Locate and identify every blood parasite.
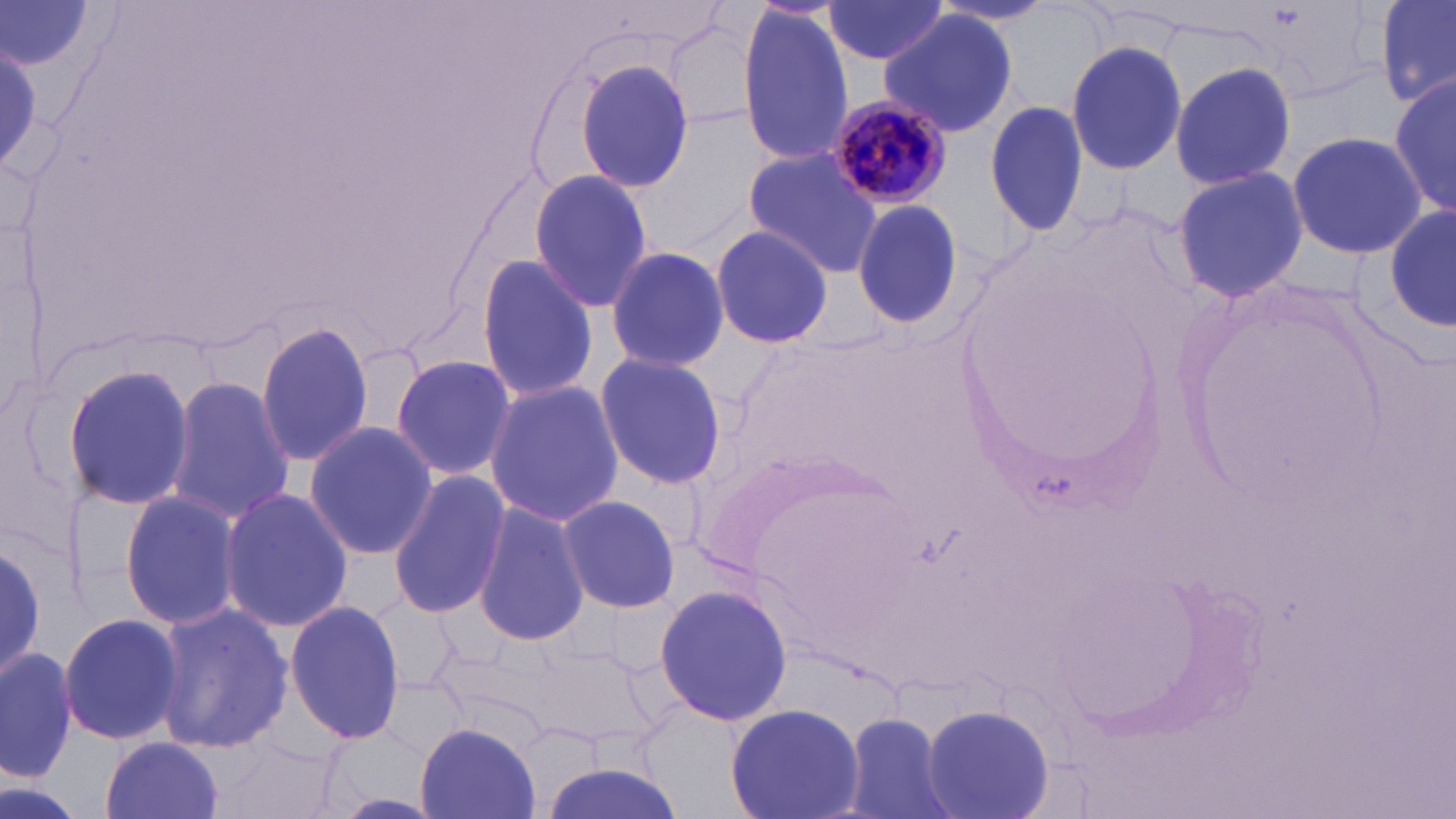

Approximate bounding boxes as (x1,y1)-(x2,y2) corner pairs in pixels.
Plasmodium malariae-infected red blood cells: (827,95)-(956,210).
No Plasmodium falciparum, Plasmodium ovale, Plasmodium vivax, Babesia divergens, or Trypanosoma brucei observed.

slide-level diagnosis = Plasmodium malariae
preparation = thin blood film
magnification = 1000x
image size = 1456×819 pixels
uninfected red blood cell locations = approximate bounding boxes as (x1,y1)-(x2,y2) corner pairs in pixels: (1375,0)-(1456,109), (819,1)-(955,66), (3,2)-(95,72), (733,8)-(858,170), (879,10)-(1020,137), (663,16)-(766,128), (1063,38)-(1189,178), (1,39)-(41,176), (1168,58)-(1298,193), (572,59)-(695,192), (1390,71)-(1455,220), (983,99)-(1091,237), (1286,129)-(1428,260), (741,148)-(884,277), (1171,166)-(1309,304), (527,169)-(655,311), (1384,199)-(1456,336), (851,200)-(966,332), (708,224)-(834,349), (603,244)-(730,373), (476,252)-(597,404), (255,321)-(377,469), (390,352)-(516,481), (594,352)-(729,490), (60,363)-(196,512), (164,376)-(295,523), (484,381)-(624,526), (303,422)-(438,559), (388,470)-(512,620), (751,479)-(908,616), (218,487)-(355,634), (121,492)-(241,630), (554,494)-(680,613), (472,500)-(590,649), (0,534)-(46,684), (652,583)-(793,727), (283,599)-(405,744), (151,601)-(295,756), (58,610)-(186,748), (519,643)-(660,752), (0,645)-(75,783), (725,702)-(863,819), (920,702)-(1055,819), (840,711)-(956,819), (416,723)-(543,817), (216,736)-(342,819), (98,737)-(225,819), (535,759)-(685,819), (0,778)-(84,819)
field of view = single
stain = May-Grünwald-Giemsa
modality = light microscopy